Assess this cell for malaria.
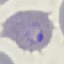
Parasitized.

Photographed with a smartphone camera at the microscope eyepiece. Giemsa-stained preparation. Thin smear of blood. Cell patch, automatically extracted from a larger field of view and resized to 64 × 64 pixels.